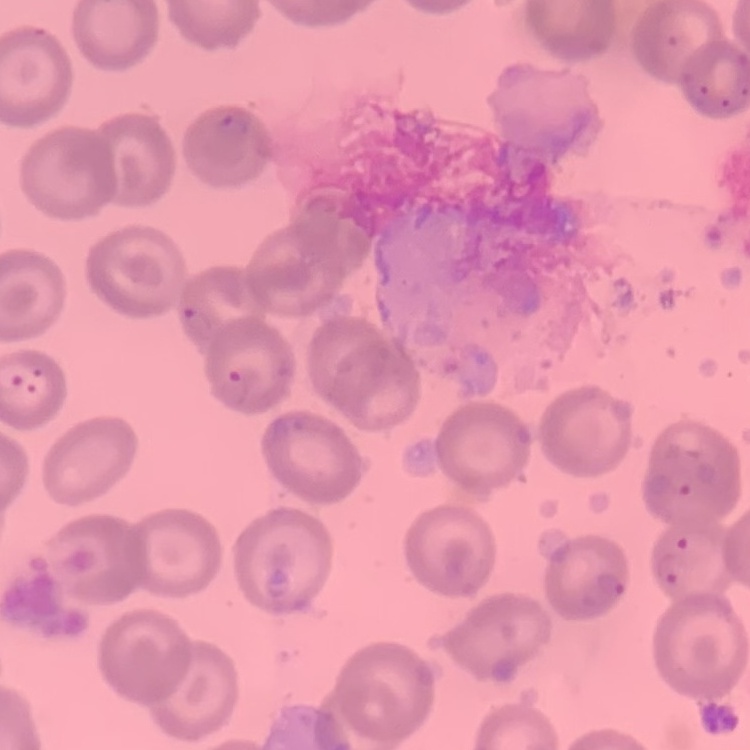 The erythrocytes show no rouleaux formation. One tile cut from a larger photomicrograph. Stained with either Field's or Giemsa. Thin blood smear.